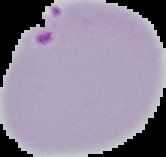

image type = cell region segmented out of the field of view; surrounding area masked to black
preparation = thin blood smear
result = Plasmodium parasites identified
image size = 166×157 pixels